Give the extent of all Trypanosoma brucei.
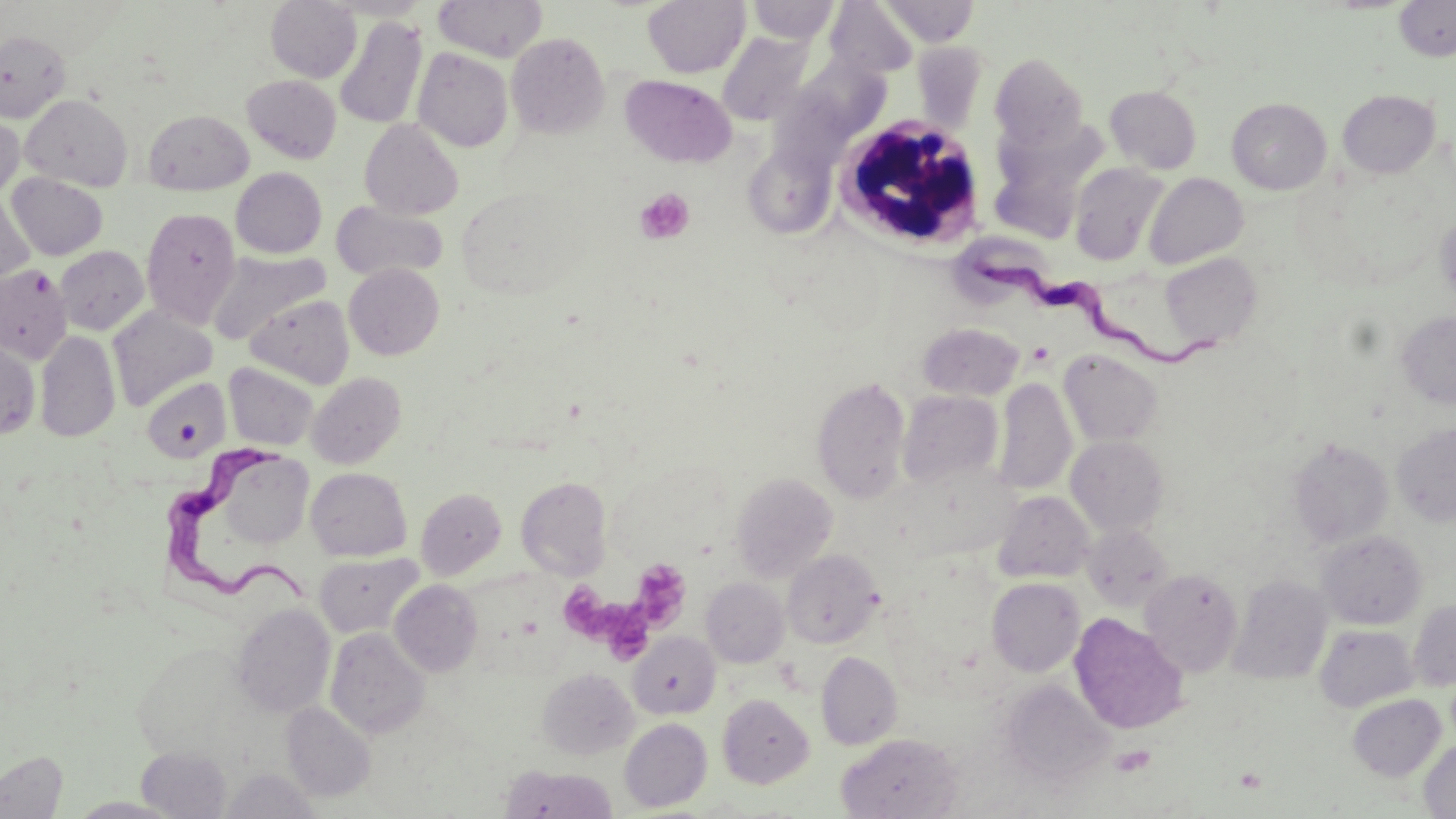
Approximate bounding boxes as (x1, y1, x2, y2) in pixels.
Trypanosoma brucei: (971, 249, 1217, 373), (161, 442, 311, 612).

{
  "slide_level_diagnosis": "Trypanosoma brucei",
  "modality": "optical microscopy",
  "stain": "May-Grünwald-Giemsa",
  "uninfected_red_blood_cell_locations": "approximate bounding boxes as (x1, y1, x2, y2) in pixels: (265, 0, 361, 83), (434, 0, 548, 62), (642, 0, 750, 78), (746, 0, 841, 44), (881, 0, 980, 46), (1394, 0, 1456, 61), (825, 1, 918, 79), (334, 16, 428, 130), (0, 30, 70, 122), (718, 31, 814, 126), (506, 33, 610, 139), (912, 41, 988, 131), (412, 48, 514, 152), (990, 52, 1088, 151), (620, 74, 736, 168), (242, 75, 342, 164), (1105, 85, 1202, 174), (1338, 89, 1441, 178), (20, 94, 132, 190), (1227, 97, 1332, 195), (143, 108, 253, 195), (0, 113, 24, 198), (359, 118, 464, 220), (988, 120, 1108, 237), (743, 145, 836, 239), (1069, 163, 1169, 266), (231, 167, 326, 258), (1143, 172, 1249, 269), (6, 173, 108, 260), (0, 191, 34, 289), (332, 202, 448, 281), (141, 206, 240, 328), (1436, 212, 1456, 302), (55, 245, 149, 335), (207, 250, 330, 343), (1159, 253, 1262, 351), (344, 263, 444, 359), (0, 264, 72, 363), (246, 294, 355, 389), (108, 306, 218, 410), (1396, 310, 1456, 409), (918, 322, 1024, 401), (36, 330, 120, 442), (0, 332, 41, 440), (1059, 349, 1163, 447), (224, 363, 319, 451), (307, 373, 406, 468), (812, 376, 911, 504), (993, 376, 1077, 495), (141, 377, 231, 463), (898, 390, 1003, 489), (1392, 423, 1456, 526), (1066, 435, 1169, 536), (1288, 437, 1394, 548), (307, 467, 412, 561), (731, 472, 837, 582), (516, 476, 612, 579), (416, 487, 507, 579), (993, 491, 1095, 583), (1080, 523, 1173, 611), (1317, 530, 1426, 629), (782, 549, 883, 648), (314, 552, 422, 638), (1139, 568, 1243, 677), (1228, 574, 1333, 685), (700, 578, 789, 667), (986, 578, 1085, 677), (390, 580, 483, 677), (1408, 601, 1456, 691), (231, 602, 336, 718), (1069, 614, 1188, 734), (1315, 624, 1418, 712), (325, 627, 430, 740), (628, 632, 721, 720), (816, 650, 902, 750), (537, 668, 638, 759), (998, 680, 1114, 786), (718, 694, 814, 788), (1347, 694, 1446, 781), (281, 702, 377, 802), (619, 718, 712, 811), (836, 732, 963, 818), (1419, 740, 1456, 818), (136, 745, 233, 818), (0, 749, 68, 818), (500, 765, 618, 818), (220, 767, 319, 818), (66, 797, 183, 818)",
  "preparation": "thin blood smear",
  "platelet_locations": "approximate bounding boxes as (x1, y1, x2, y2) in pixels: (635, 188, 695, 245), (634, 564, 692, 632), (560, 585, 617, 641), (605, 601, 652, 660), (1111, 745, 1156, 777)",
  "image_size": "1456×819 pixels",
  "field_of_view": "single",
  "white_blood_cell_locations": "approximate bounding boxes as (x1, y1, x2, y2) in pixels: (832, 113, 990, 250)",
  "magnification": "1000x"
}